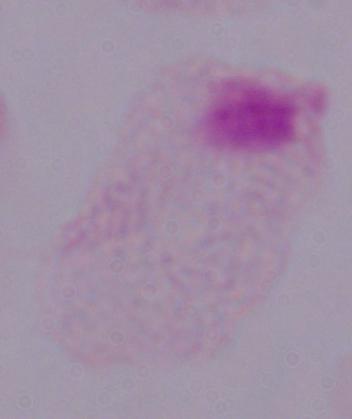
A trichomonad is shown. 1000x magnification. Micrograph.